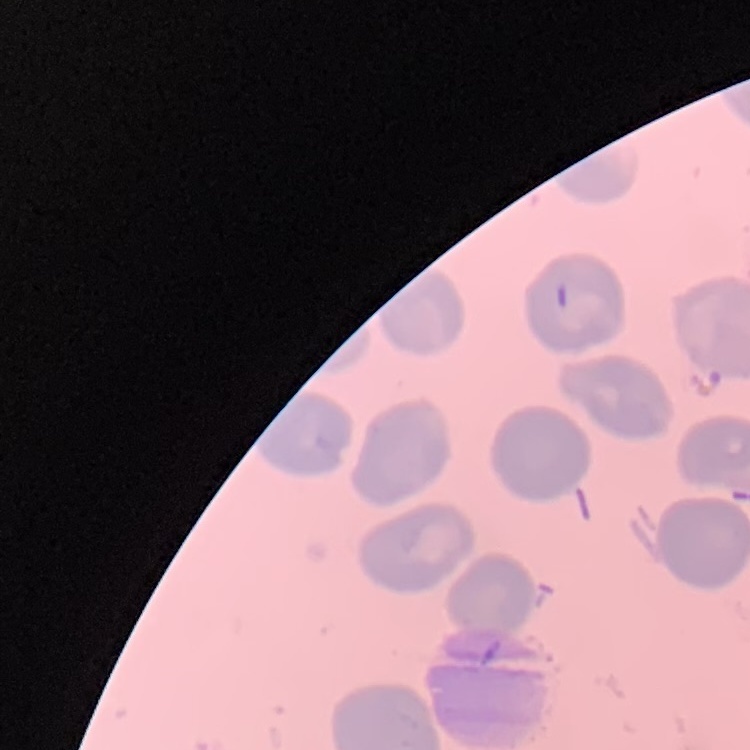
Summary:
  - Red blood cell morphology: no rouleaux formation
  - Preparation: thin blood smear
  - Image type: one tile cut from a larger photomicrograph
  - Stain: Field's or Giemsa